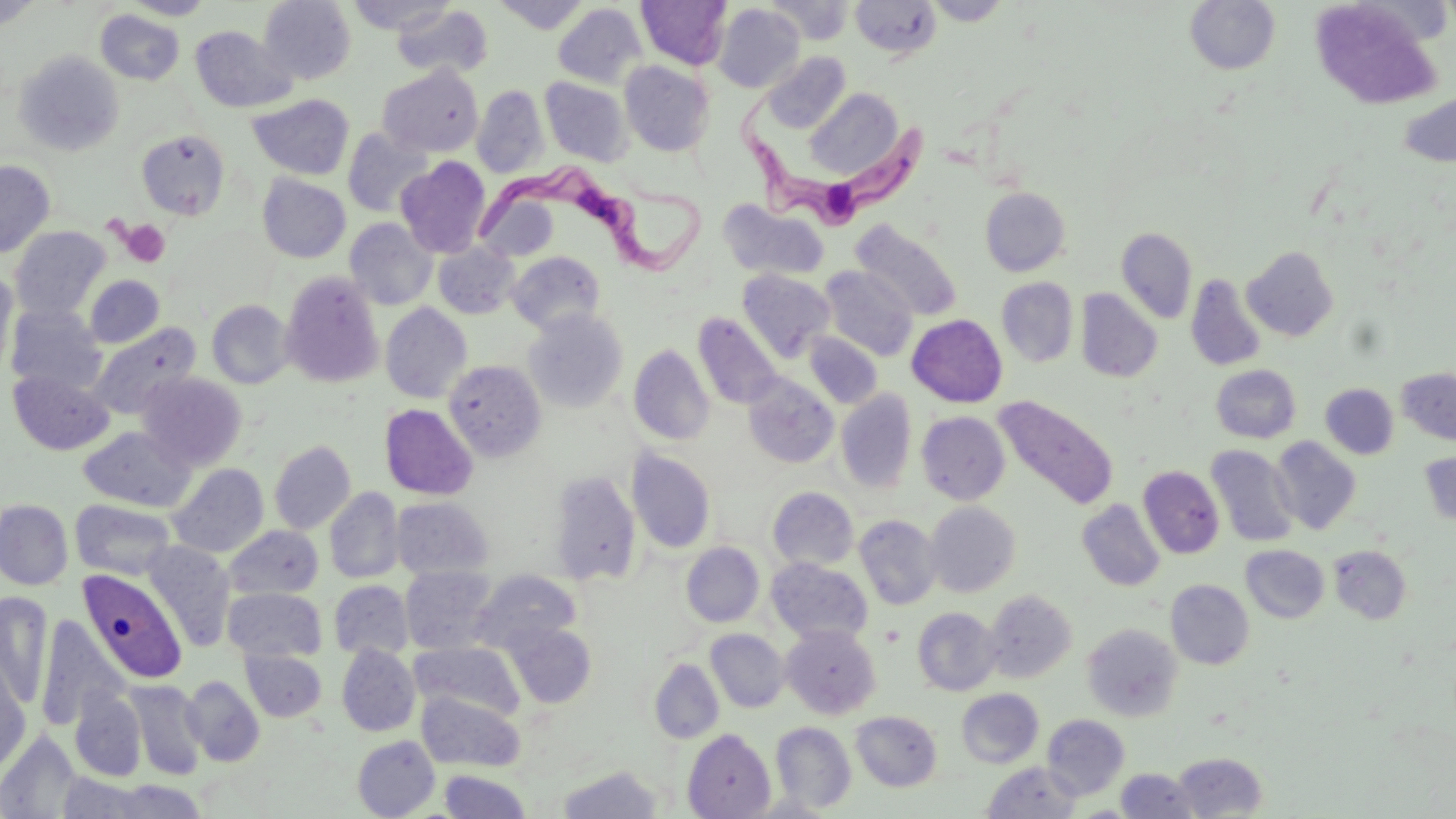
slide-level diagnosis = Trypanosoma brucei
preparation = thin blood smear
Trypanosoma brucei locations = approximate bounding boxes as named x1/y1/x2/y2 corners in pixels: (x1=740, y1=92, x2=934, y2=229), (x1=476, y1=156, x2=709, y2=282)
image size = 1456×819 pixels
field of view = one of a larger specimen
stain = May-Grünwald-Giemsa
platelet locations = approximate bounding boxes as named x1/y1/x2/y2 corners in pixels: (x1=120, y1=220, x2=171, y2=267)
modality = optical microscopy
uninfected red blood cell locations = approximate bounding boxes as named x1/y1/x2/y2 corners in pixels: (x1=122, y1=0, x2=216, y2=19), (x1=259, y1=0, x2=356, y2=85), (x1=347, y1=0, x2=454, y2=35), (x1=492, y1=0, x2=591, y2=33), (x1=513, y1=0, x2=629, y2=48), (x1=635, y1=0, x2=732, y2=70), (x1=766, y1=0, x2=854, y2=44), (x1=851, y1=0, x2=942, y2=59), (x1=923, y1=0, x2=1012, y2=26), (x1=0, y1=1, x2=41, y2=31), (x1=1184, y1=1, x2=1281, y2=75), (x1=1309, y1=2, x2=1444, y2=109), (x1=552, y1=3, x2=646, y2=88), (x1=392, y1=4, x2=493, y2=80), (x1=713, y1=4, x2=804, y2=93), (x1=95, y1=10, x2=184, y2=85), (x1=190, y1=26, x2=297, y2=114), (x1=14, y1=51, x2=124, y2=156), (x1=761, y1=52, x2=850, y2=133), (x1=619, y1=61, x2=715, y2=156), (x1=378, y1=65, x2=484, y2=157), (x1=539, y1=76, x2=632, y2=167), (x1=472, y1=85, x2=549, y2=178), (x1=805, y1=89, x2=904, y2=180), (x1=1399, y1=91, x2=1455, y2=167), (x1=248, y1=94, x2=354, y2=180), (x1=342, y1=127, x2=432, y2=218), (x1=136, y1=130, x2=230, y2=220), (x1=395, y1=157, x2=491, y2=258), (x1=0, y1=160, x2=55, y2=258), (x1=257, y1=174, x2=351, y2=263), (x1=980, y1=187, x2=1070, y2=276), (x1=718, y1=200, x2=830, y2=280), (x1=345, y1=218, x2=438, y2=310), (x1=851, y1=220, x2=963, y2=321), (x1=10, y1=226, x2=110, y2=319), (x1=1116, y1=227, x2=1197, y2=324), (x1=433, y1=242, x2=519, y2=319), (x1=1242, y1=246, x2=1338, y2=341), (x1=506, y1=250, x2=606, y2=334), (x1=819, y1=265, x2=918, y2=361), (x1=0, y1=269, x2=18, y2=378), (x1=737, y1=269, x2=835, y2=363), (x1=280, y1=272, x2=384, y2=388), (x1=85, y1=275, x2=164, y2=348), (x1=1186, y1=275, x2=1266, y2=372), (x1=996, y1=278, x2=1078, y2=367), (x1=1076, y1=289, x2=1162, y2=382), (x1=207, y1=300, x2=294, y2=389), (x1=380, y1=303, x2=472, y2=403), (x1=5, y1=304, x2=107, y2=396), (x1=523, y1=309, x2=628, y2=413), (x1=693, y1=312, x2=783, y2=411), (x1=907, y1=314, x2=1007, y2=407), (x1=87, y1=322, x2=202, y2=420), (x1=804, y1=332, x2=882, y2=409), (x1=628, y1=344, x2=715, y2=446), (x1=444, y1=359, x2=546, y2=462), (x1=1211, y1=365, x2=1301, y2=443), (x1=1396, y1=368, x2=1456, y2=445), (x1=8, y1=371, x2=114, y2=455), (x1=137, y1=372, x2=247, y2=471), (x1=743, y1=373, x2=839, y2=468), (x1=1320, y1=384, x2=1398, y2=459), (x1=836, y1=389, x2=916, y2=494), (x1=993, y1=395, x2=1119, y2=511), (x1=380, y1=404, x2=478, y2=500), (x1=916, y1=411, x2=1010, y2=504), (x1=79, y1=426, x2=196, y2=512), (x1=1270, y1=437, x2=1361, y2=534), (x1=269, y1=440, x2=356, y2=535), (x1=1206, y1=445, x2=1300, y2=548), (x1=627, y1=450, x2=715, y2=553), (x1=1418, y1=452, x2=1456, y2=527), (x1=167, y1=463, x2=268, y2=557), (x1=1138, y1=466, x2=1224, y2=559), (x1=549, y1=471, x2=641, y2=585), (x1=767, y1=487, x2=858, y2=571), (x1=324, y1=488, x2=404, y2=583), (x1=391, y1=496, x2=493, y2=579), (x1=0, y1=499, x2=73, y2=589), (x1=71, y1=499, x2=176, y2=580), (x1=1076, y1=499, x2=1165, y2=591), (x1=925, y1=501, x2=1021, y2=597), (x1=855, y1=515, x2=941, y2=610), (x1=224, y1=526, x2=324, y2=600), (x1=143, y1=541, x2=236, y2=651), (x1=681, y1=542, x2=764, y2=627), (x1=1241, y1=545, x2=1329, y2=623), (x1=1329, y1=546, x2=1413, y2=623), (x1=766, y1=558, x2=873, y2=645), (x1=400, y1=566, x2=499, y2=655), (x1=79, y1=568, x2=189, y2=684), (x1=469, y1=570, x2=581, y2=655), (x1=1166, y1=579, x2=1254, y2=669), (x1=329, y1=580, x2=413, y2=660), (x1=223, y1=587, x2=326, y2=662), (x1=983, y1=590, x2=1077, y2=683), (x1=0, y1=592, x2=52, y2=708), (x1=912, y1=607, x2=1001, y2=695), (x1=35, y1=616, x2=127, y2=728), (x1=504, y1=622, x2=597, y2=708), (x1=1082, y1=624, x2=1182, y2=721), (x1=782, y1=625, x2=881, y2=719), (x1=706, y1=629, x2=790, y2=713), (x1=410, y1=642, x2=524, y2=721), (x1=336, y1=644, x2=420, y2=736), (x1=241, y1=649, x2=326, y2=721), (x1=649, y1=658, x2=724, y2=744), (x1=0, y1=660, x2=31, y2=775), (x1=181, y1=676, x2=265, y2=766), (x1=125, y1=680, x2=208, y2=780), (x1=70, y1=688, x2=148, y2=781), (x1=956, y1=689, x2=1043, y2=768), (x1=416, y1=692, x2=525, y2=772), (x1=851, y1=711, x2=942, y2=792), (x1=1041, y1=714, x2=1130, y2=800), (x1=771, y1=721, x2=857, y2=813), (x1=682, y1=728, x2=776, y2=818), (x1=0, y1=730, x2=84, y2=819), (x1=352, y1=736, x2=440, y2=818), (x1=1172, y1=752, x2=1268, y2=818), (x1=981, y1=762, x2=1082, y2=818), (x1=556, y1=765, x2=663, y2=818), (x1=1115, y1=769, x2=1200, y2=818), (x1=438, y1=770, x2=532, y2=818), (x1=56, y1=773, x2=151, y2=818), (x1=100, y1=779, x2=209, y2=819)
magnification = 1000x